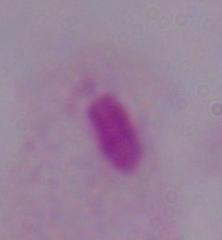
Summary:
  - Identification: trichomonad
  - Magnification: 1000x
  - Modality: photomicrograph